Name the parasite shown.
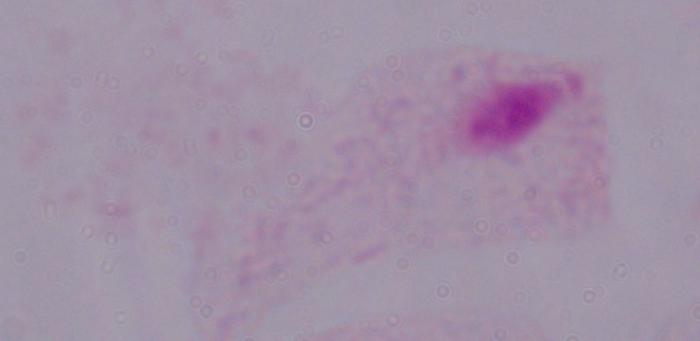

This is a trichomonad.

Captured at 1000x magnification. Micrograph.